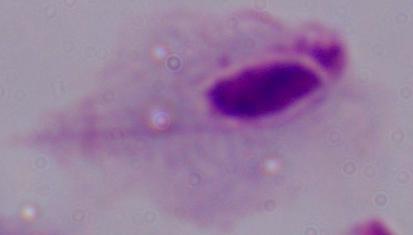
Summary:
  - Magnification: 1000x
  - Identification: trichomonad
  - Modality: photomicrograph